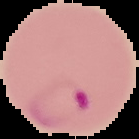 Segmented cell region on a black background. From a thin blood smear. Malaria status: parasitized. Image is 139×139 pixels.